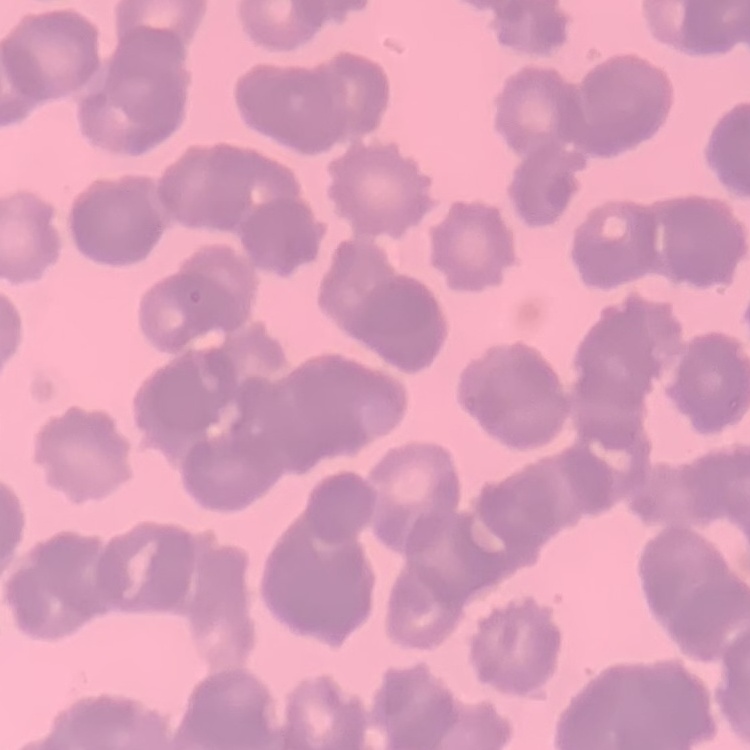 The erythrocytes show rouleaux formation. Field's or Giemsa stain. Square crop of a larger photomicrograph. Thin blood smear.